Locate malaria parasites and identify their life-cycle stages.
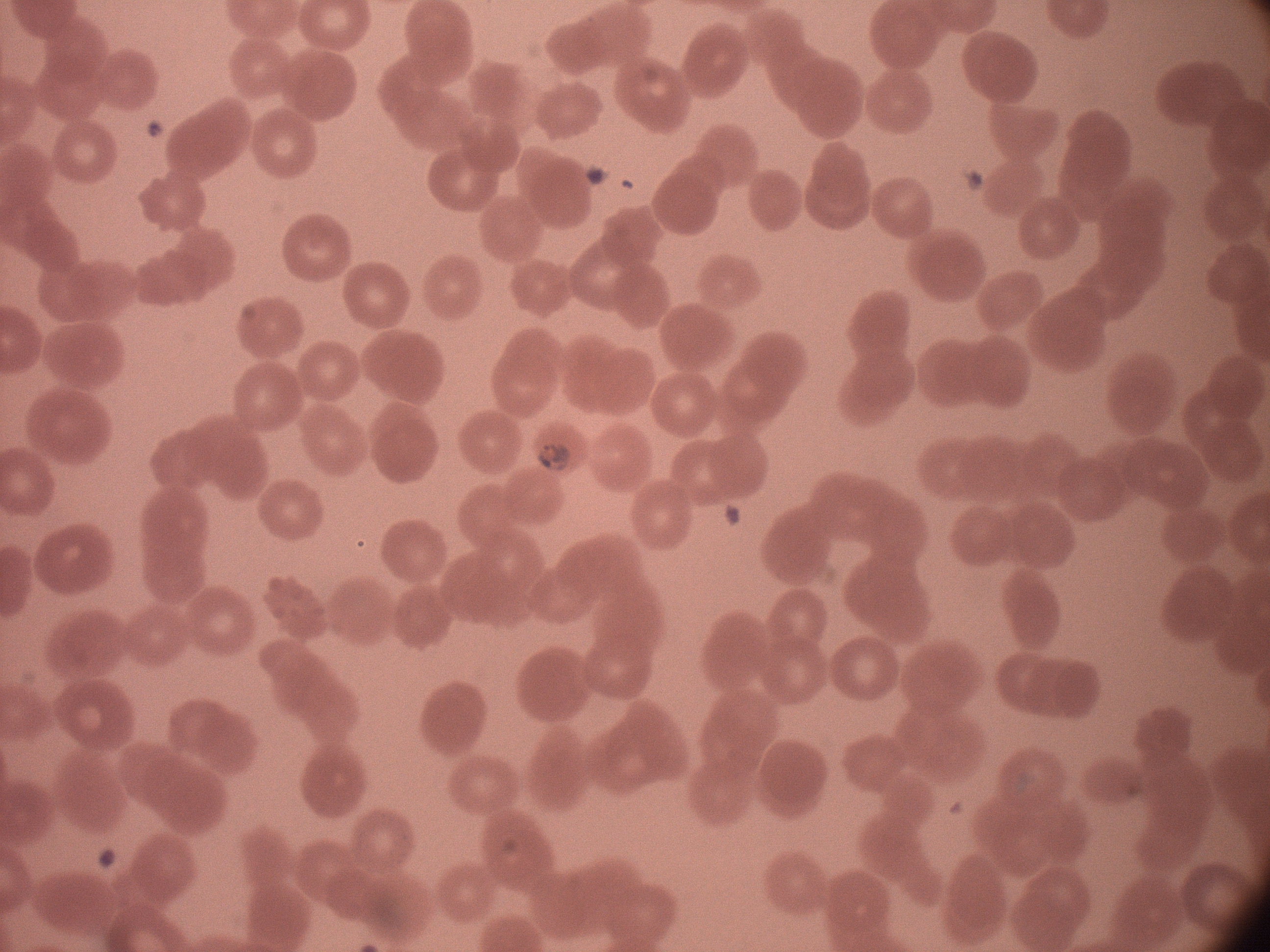

Approximate bounding boxes as named x1/y1/x2/y2 corners in pixels, from the source annotation, which is not necessarily exhaustive.
Trophozoites: (x1=533, y1=436, x2=577, y2=479).

Summary:
  - Field of view: one from this slide
  - Image size: 1270×952 pixels
  - Magnification: 100x
  - Stain: Giemsa
  - Species: Plasmodium falciparum
  - Preparation: thin blood smear
  - Microscope: Leica DM2000 with built-in camera